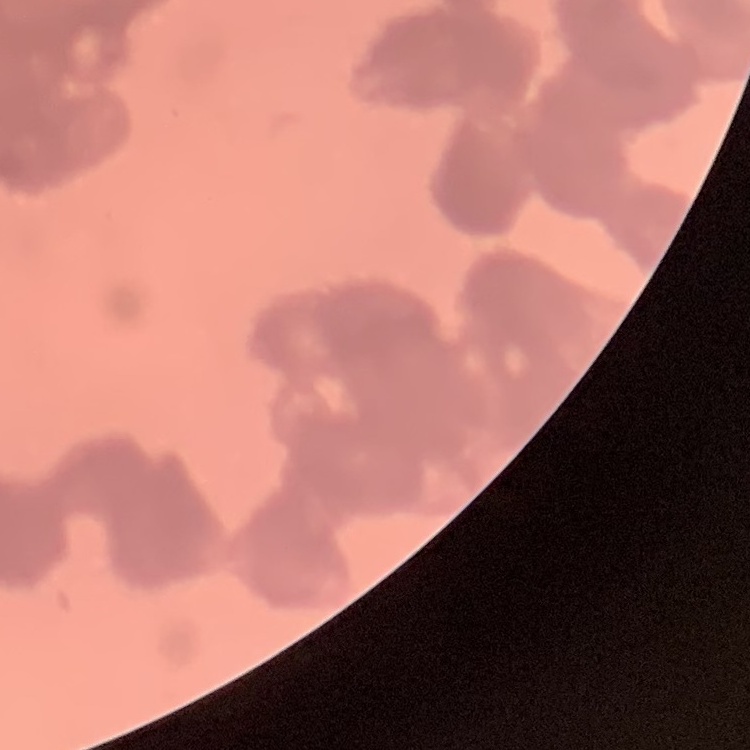
The red blood cells exhibit rouleaux formation. Square crop of a larger photomicrograph. Thin blood smear. Field's or Giemsa stain.